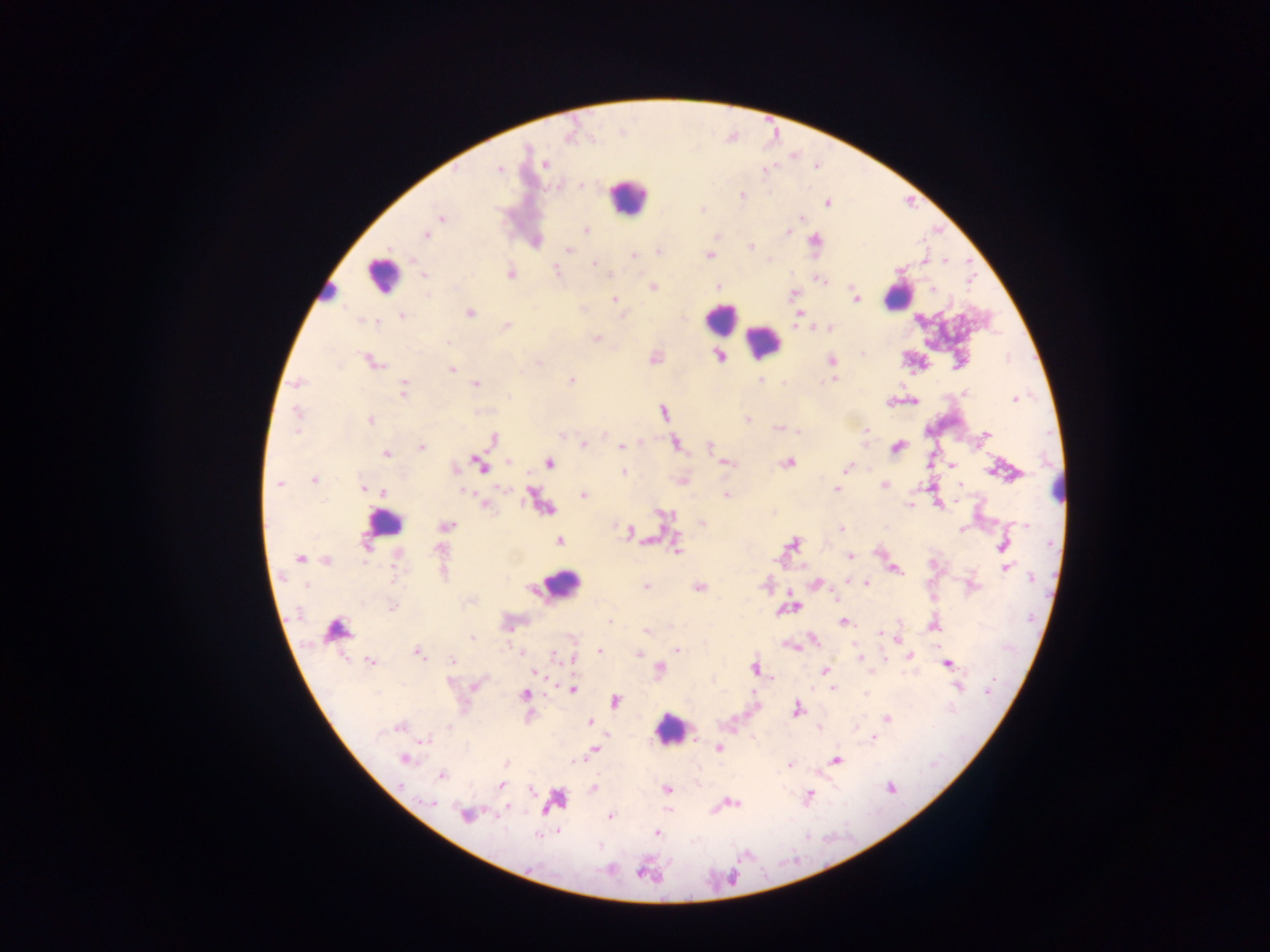

Approximate centers as (x, y) in pixels.
Summary:
  - Leukocyte locations: (628, 198), (382, 275), (329, 290), (899, 296), (720, 317), (763, 342), (1059, 486), (385, 523), (561, 585), (337, 629), (671, 729)
  - Plasmodium parasite locations: (499, 168), (766, 170), (742, 195), (827, 204), (441, 218), (801, 218), (586, 229), (788, 232), (425, 236), (751, 247), (568, 250), (633, 255), (709, 255), (944, 261), (594, 263), (557, 271), (511, 273), (424, 276), (822, 280), (719, 286), (653, 288), (933, 290), (794, 294), (856, 298), (615, 299), (582, 310), (470, 312), (798, 314), (402, 316), (372, 322), (506, 326), (794, 326), (829, 327), (596, 338), (718, 356), (831, 360), (373, 362), (539, 363), (452, 369), (760, 379), (833, 379), (572, 381), (298, 383), (476, 384), (404, 388), (965, 393), (509, 396), (1015, 398), (297, 412), (664, 412), (747, 419), (370, 421), (776, 427), (797, 431), (867, 431), (562, 435), (986, 435), (493, 439), (584, 443), (676, 443), (421, 446), (710, 446), (622, 447), (896, 448), (386, 453), (509, 462), (727, 463), (789, 463), (550, 464), (951, 465), (480, 466), (846, 468), (455, 469), (623, 472), (314, 480), (278, 484), (960, 484), (885, 485), (363, 487), (837, 490), (384, 492), (464, 492), (584, 494), (727, 495), (956, 502), (486, 505), (910, 506), (666, 515), (702, 523), (1025, 525), (446, 526), (841, 529), (961, 530), (629, 531), (559, 541), (367, 544), (792, 544), (1003, 546), (677, 549), (439, 551), (850, 556), (299, 558), (326, 560), (1006, 567), (895, 570), (395, 576), (1032, 578), (847, 581), (867, 583), (815, 584), (646, 586), (699, 587), (789, 592), (834, 598), (392, 606), (609, 621), (843, 622), (934, 627), (647, 631), (880, 632), (472, 638), (812, 638), (791, 646), (677, 650), (600, 651), (417, 653), (638, 653), (555, 656), (910, 656), (860, 657), (572, 659), (452, 660), (370, 661), (947, 663), (660, 669), (755, 669), (824, 671), (538, 672), (450, 682), (476, 685), (958, 687), (832, 688), (573, 690), (988, 693), (867, 694), (524, 695), (616, 701), (796, 709), (887, 719), (590, 721), (449, 727), (397, 728), (873, 738), (426, 740), (718, 749), (595, 750), (404, 760), (837, 760), (507, 764), (789, 764), (442, 775), (502, 785), (593, 787), (891, 787), (667, 789), (532, 790), (809, 796), (430, 802), (733, 803), (507, 806), (465, 814), (610, 816), (558, 831), (657, 832), (538, 834)
  - Field of view: single
  - Capture: mobile-phone photograph through a microscope
  - Country: Ghana
  - Preparation: thick blood smear
  - Image size: 1270×952 pixels